Report the malaria status of this cell.
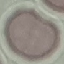
It is uninfected.

Summary:
  - Image type: automatically extracted cell patch, resized to 64 × 64 pixels
  - Preparation: thin blood film
  - Capture: smartphone through the microscope eyepiece
  - Stain: Giemsa